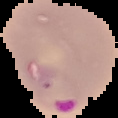 From a thin blood film. The area outside the segmented cell region is set to black. Image is 118×118 pixels. Result: malaria parasites detected.